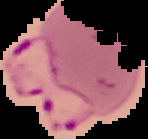
{
  "malaria_status": "parasitized",
  "preparation": "thin blood film",
  "image_type": "cell region segmented out of the field of view; surrounding area masked to black",
  "image_size": "148×139 pixels"
}